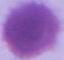

{
  "magnification": "1000x",
  "identification": "red blood cell",
  "modality": "micrograph"
}